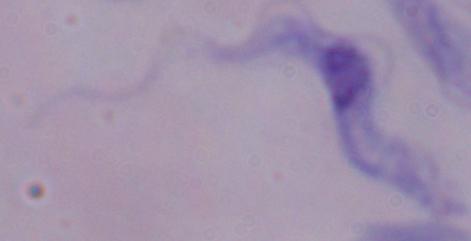

Summary:
  - Identification: trypanosome
  - Modality: photomicrograph
  - Magnification: 1000x